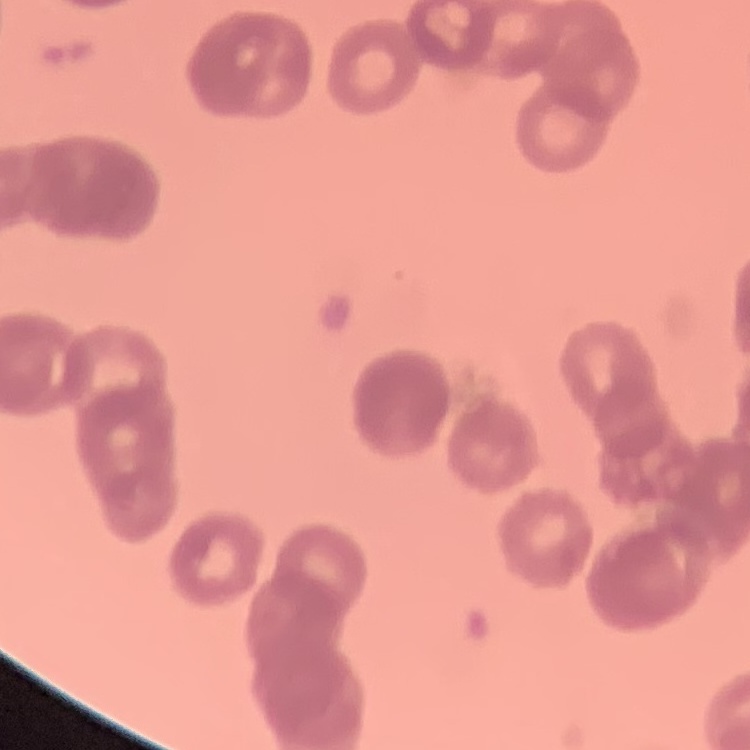

The red blood cells exhibit rouleaux formation. Square crop of a larger photomicrograph. Stained with either Field's or Giemsa. Thin blood smear.